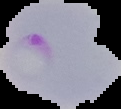 Image is 121×109 pixels. Result: Plasmodium parasites identified. Segmented cell region on a black background. From a thin blood film.